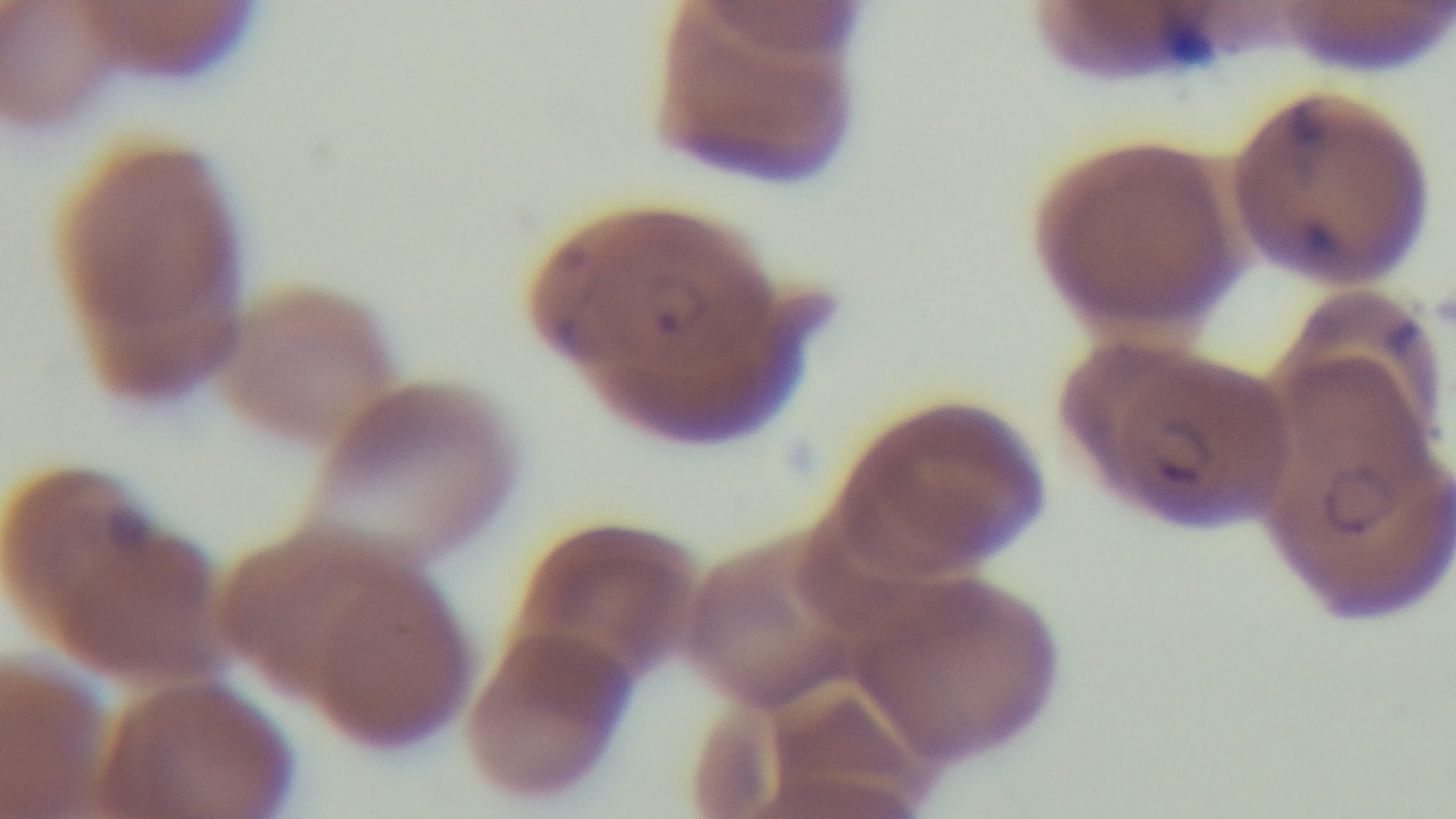

Summary:
  - Stain: Giemsa
  - Objective: 100x oil immersion
  - Malaria status: positive
  - Preparation: thin
  - Capture: mounted 4K digital camera
  - Field of view: one from the slide
  - Modality: light microscopy